Name the blood parasite species.
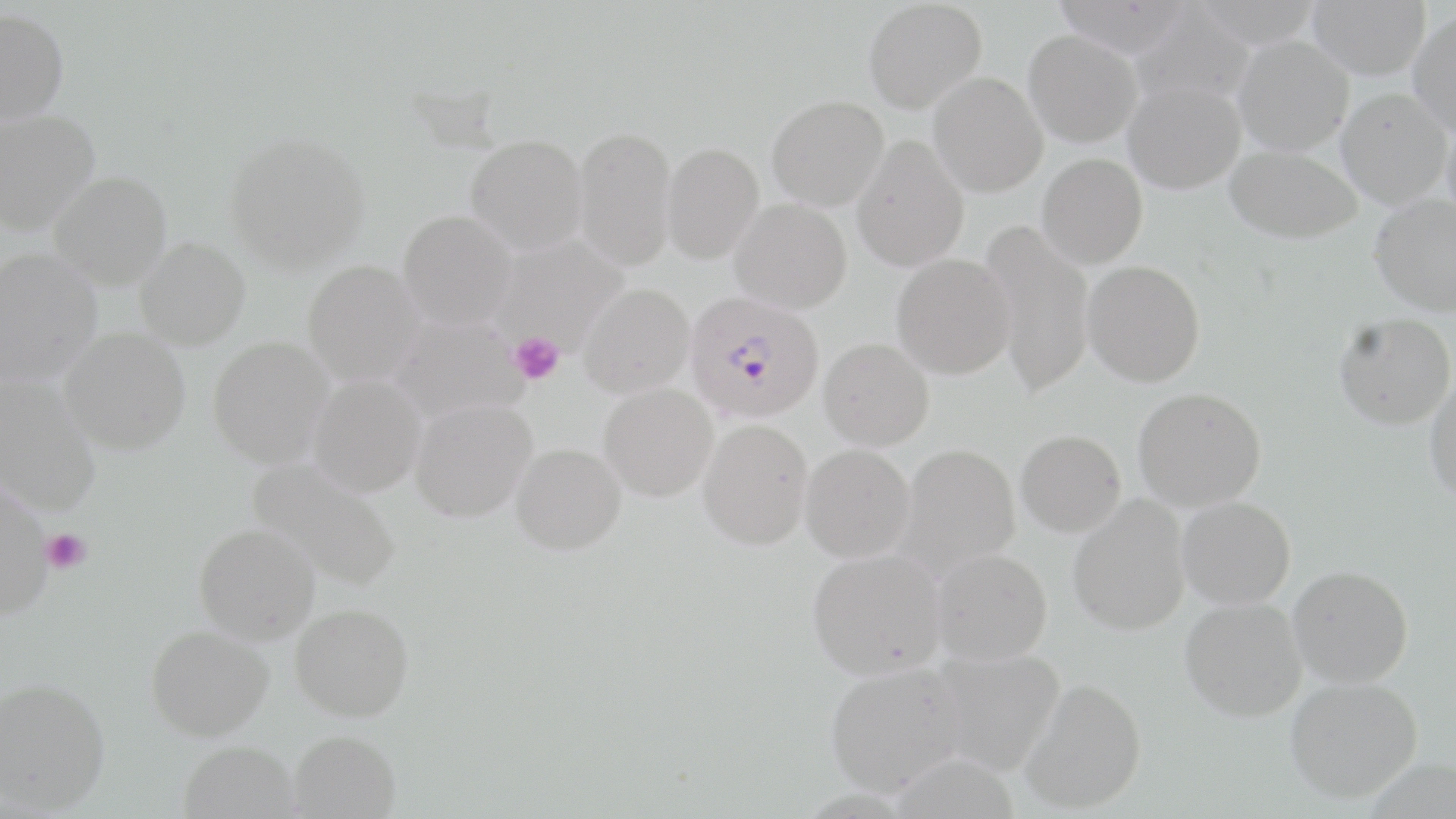

Plasmodium falciparum.

platelet_locations: 'approximate bounding boxes as (x1, y1, x2, y2) in pixels: (510, 333, 564, 386), (41, 530, 91, 573)'
magnification: 1000x
modality: optical microscopy
field_of_view: single
plasmodium_falciparum_infected_red_blood_cell_locations: 'approximate bounding boxes as (x1, y1, x2, y2) in pixels: (685, 291, 825, 423)'
preparation: thin blood smear
image_size: 1456×819 pixels
stain: May-Grünwald-Giemsa
uninfected_red_blood_cell_locations: 'approximate bounding boxes as (x1, y1, x2, y2) in pixels: (863, 0, 986, 113), (1051, 0, 1193, 55), (1193, 0, 1325, 47), (1308, 0, 1430, 79), (1129, 5, 1257, 110), (0, 7, 69, 126), (1408, 8, 1456, 137), (1024, 30, 1143, 147), (1233, 34, 1353, 155), (928, 71, 1048, 197), (1124, 80, 1245, 194), (1337, 87, 1452, 209), (767, 94, 889, 210), (0, 109, 99, 233), (1442, 109, 1456, 228), (574, 125, 677, 270), (224, 131, 371, 272), (465, 134, 588, 254), (852, 134, 969, 271), (662, 141, 764, 264), (1225, 144, 1362, 243), (1037, 153, 1147, 268), (49, 172, 172, 289), (1370, 194, 1456, 316), (730, 199, 852, 314), (397, 209, 516, 330), (979, 220, 1095, 396), (490, 236, 628, 355), (135, 237, 250, 350), (1, 248, 102, 385), (892, 253, 1015, 379), (301, 260, 425, 387), (1082, 260, 1205, 387), (578, 282, 694, 397), (1334, 312, 1456, 430), (391, 315, 528, 423), (60, 328, 190, 454), (207, 336, 335, 469), (819, 338, 934, 450), (307, 373, 426, 498), (0, 376, 101, 515), (1425, 376, 1456, 505), (600, 383, 717, 501), (1133, 387, 1266, 511), (410, 397, 537, 521), (698, 419, 812, 550), (1016, 429, 1126, 536), (511, 442, 626, 555), (895, 443, 1020, 577), (800, 444, 915, 563), (246, 458, 403, 592), (0, 475, 54, 619), (1068, 496, 1191, 636), (1177, 496, 1296, 609), (193, 523, 320, 644), (807, 548, 946, 680), (931, 548, 1052, 665), (1288, 565, 1413, 687), (1180, 596, 1308, 721), (290, 603, 414, 721), (145, 625, 274, 741), (927, 647, 1065, 776), (824, 663, 966, 797), (0, 677, 110, 813), (1284, 677, 1422, 802), (1021, 678, 1147, 814), (288, 729, 401, 818), (179, 741, 300, 819)'